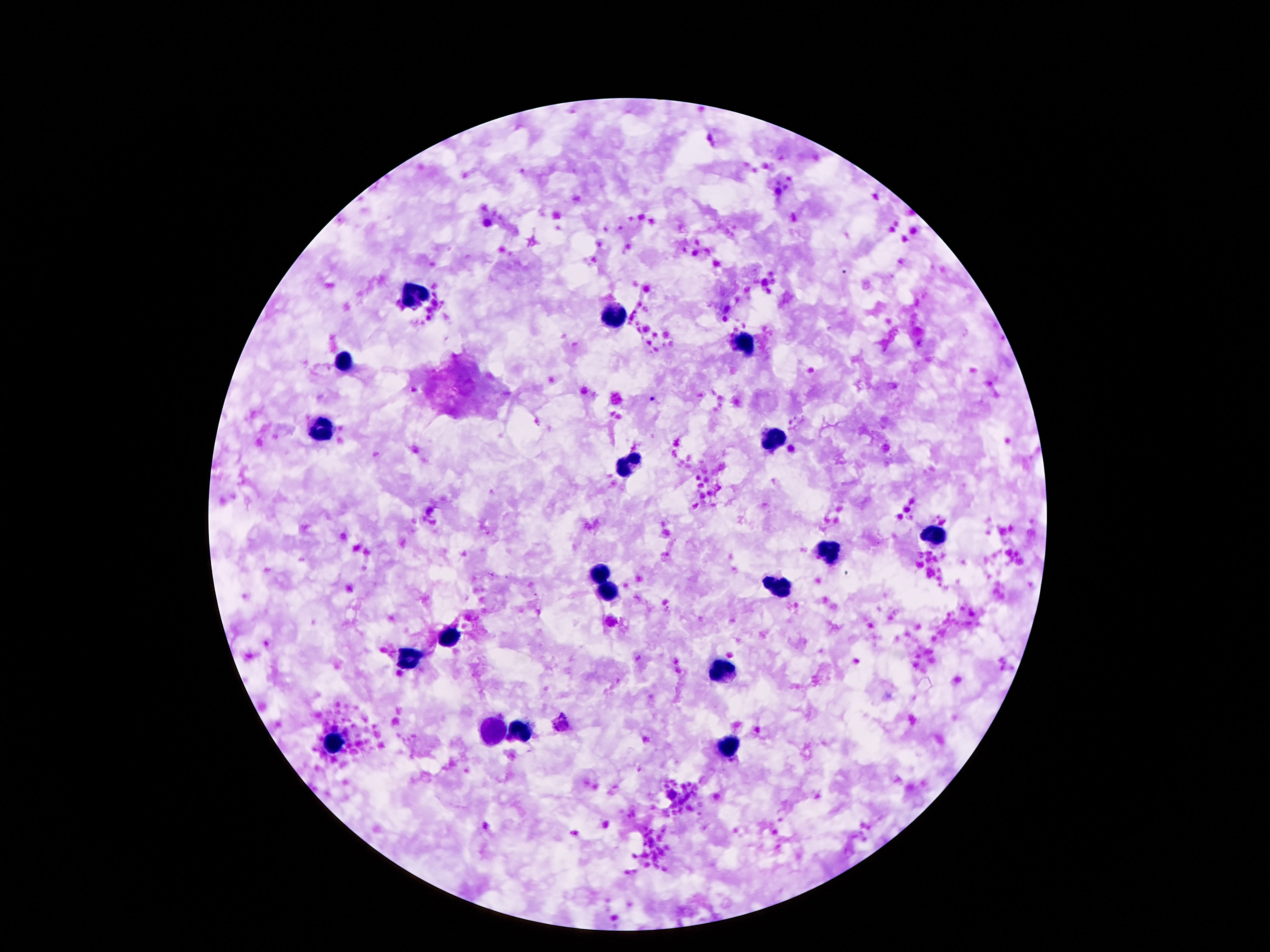

field of view = one from this slide
magnification = 100x
preparation = thick blood smear
stain = Giemsa
image size = 1270×952 pixels
leukocyte locations = approximate centers as [x, y] in pixels: [412, 294], [610, 316], [743, 343], [342, 362], [321, 431], [771, 438], [626, 466], [934, 536], [832, 551], [601, 573], [782, 586], [607, 591], [448, 636], [408, 659], [721, 671], [519, 732], [333, 743], [728, 748]
patient malaria status = not infected
capture = smartphone camera through the microscope eyepiece